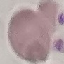

{
  "result": "no malaria parasites detected",
  "image_type": "automatically extracted cell patch, resized to 64 × 64 pixels",
  "capture": "smartphone through the microscope eyepiece",
  "stain": "Giemsa",
  "preparation": "thin blood smear"
}